Assess this cell for malaria.
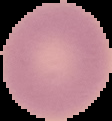

It is uninfected.

{
  "image_size": "112×121 pixels",
  "image_type": "segmented cell region with the area outside set to black",
  "preparation": "thin blood smear"
}